Assess this cell for malaria.
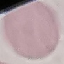
Uninfected.

Summary:
  - Stain: Giemsa
  - Image type: automatically extracted cell patch, resized to 64 × 64 pixels
  - Preparation: thin blood smear
  - Capture: smartphone through the microscope eyepiece